Locate every blood parasite and identify its species.
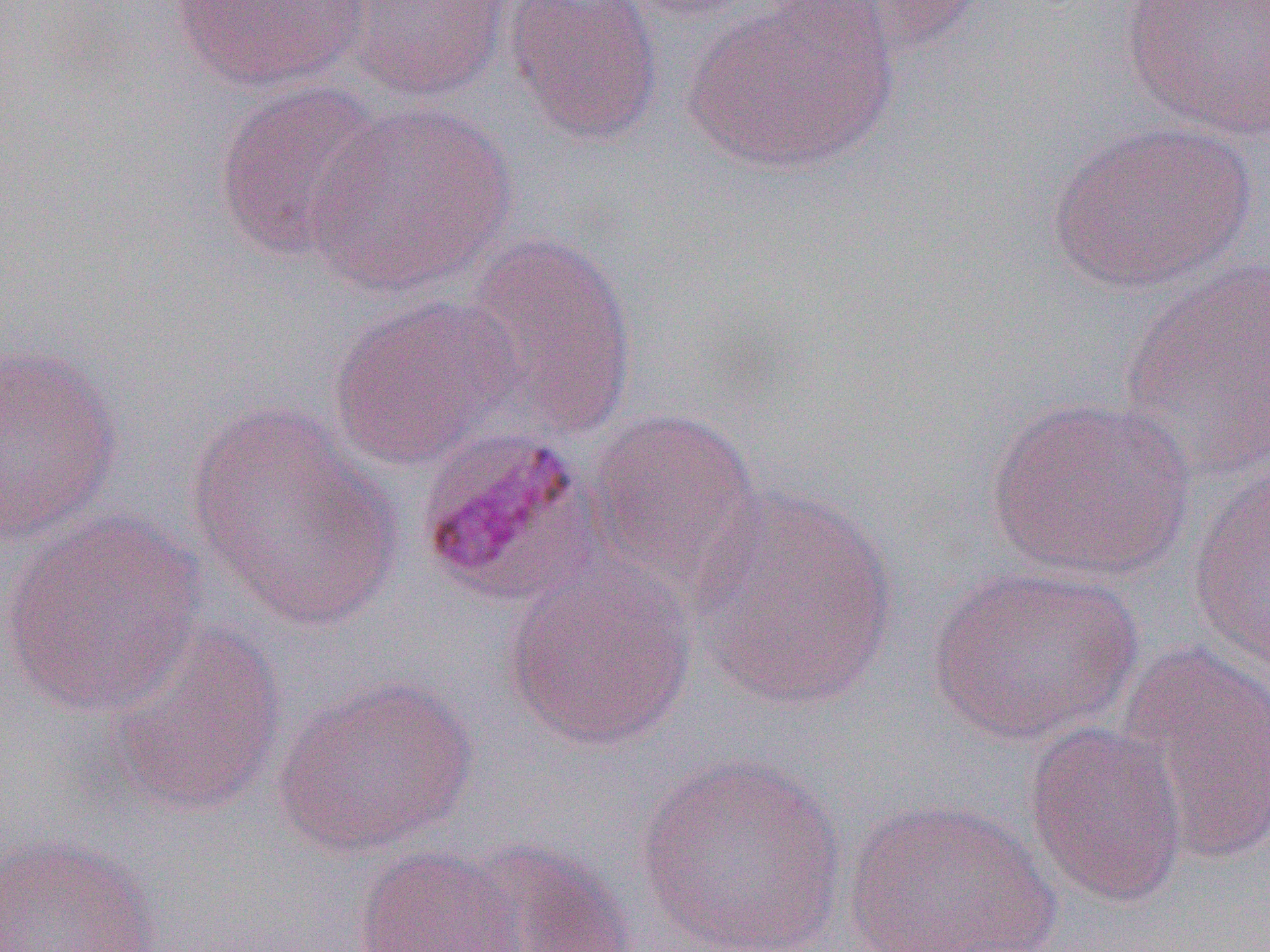
Approximate bounding boxes as (x1, y1, x2, y2) in pixels.
Plasmodium malariae-infected red blood cells: (412, 426, 593, 605).
No Plasmodium falciparum, Plasmodium ovale, Plasmodium vivax, Babesia divergens, or Trypanosoma brucei observed.

slide_level_diagnosis: Plasmodium malariae
preparation: thin blood smear
modality: light microscopy
magnification: 1000x
uninfected_red_blood_cell_locations: 'approximate bounding boxes as (x1, y1, x2, y2) in pixels: (170, 0, 370, 93), (344, 0, 510, 102), (504, 0, 664, 146), (619, 0, 767, 23), (787, 0, 988, 64), (1118, 0, 1270, 142), (684, 1, 899, 176), (212, 80, 385, 262), (306, 101, 518, 296), (1048, 119, 1257, 294), (456, 230, 639, 436), (1119, 256, 1270, 485), (327, 295, 521, 470), (0, 344, 123, 545), (984, 395, 1197, 583), (186, 404, 401, 630), (584, 406, 763, 592), (1186, 466, 1270, 671), (686, 482, 899, 710), (0, 511, 207, 717), (502, 556, 697, 753), (924, 563, 1145, 744), (106, 620, 289, 819), (1114, 641, 1270, 866), (273, 674, 477, 858), (1022, 720, 1190, 908), (635, 754, 849, 952), (841, 798, 1061, 952), (0, 833, 161, 952), (450, 837, 637, 952), (352, 845, 527, 952)'
image_size: 1270×952 pixels
field_of_view: single